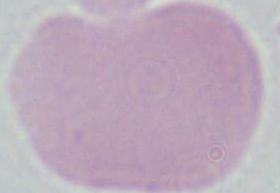
{
  "modality": "photomicrograph",
  "magnification": "1000x",
  "identification": "red blood cell"
}